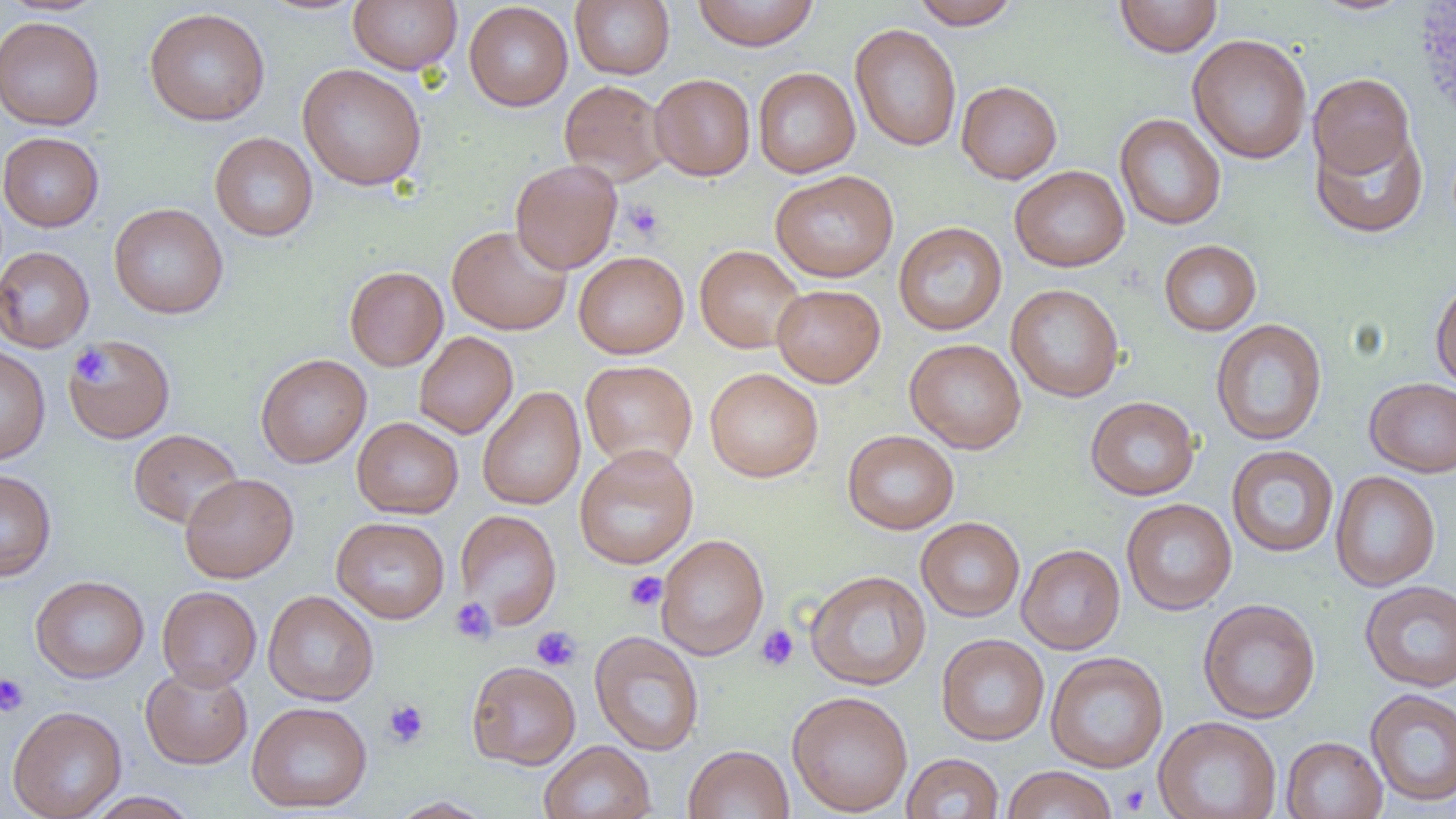

Approximate bounding boxes as (x1,y1)-(x2,y2) corner pairs in pixels. Uninfected red blood cell locations: (348,0)-(462,74), (691,0)-(820,51), (911,0)-(1020,29), (1114,0)-(1223,57), (1310,0)-(1417,16), (570,1)-(675,79), (463,2)-(573,111), (144,7)-(271,126), (1,15)-(104,131), (850,24)-(962,152), (1187,33)-(1312,165), (297,63)-(427,191), (753,67)-(860,178), (763,69)-(872,282), (1307,73)-(1415,179), (649,74)-(755,180), (559,79)-(669,185), (956,80)-(1062,183), (1115,113)-(1226,230), (1311,126)-(1427,238), (0,132)-(104,231), (209,132)-(318,242), (510,159)-(623,274), (1009,165)-(1130,272), (770,170)-(899,282), (108,203)-(229,319), (893,221)-(1007,336), (447,224)-(571,335), (1159,240)-(1262,336), (694,245)-(806,353), (0,246)-(94,353), (573,251)-(689,359), (344,265)-(448,371), (1430,277)-(1456,393), (1006,283)-(1125,402), (771,284)-(885,388), (1210,318)-(1327,446), (414,331)-(518,438), (63,335)-(177,444), (904,338)-(1026,453), (0,345)-(51,464), (255,353)-(371,468), (580,360)-(698,470), (704,368)-(823,482), (1364,377)-(1456,477), (477,386)-(586,511), (1085,396)-(1201,500), (352,417)-(464,519), (128,429)-(243,529), (842,429)-(959,534), (574,444)-(698,569), (1226,445)-(1339,558), (0,469)-(57,581), (1330,470)-(1441,591), (180,473)-(299,583), (1121,498)-(1237,615), (454,509)-(562,629), (331,516)-(450,623), (915,516)-(1025,621), (655,534)-(769,661), (1016,543)-(1125,654), (804,569)-(931,690), (30,575)-(149,683), (1359,579)-(1456,692), (157,586)-(262,690), (262,590)-(379,706), (1197,598)-(1321,724), (589,631)-(704,756), (936,633)-(1050,745), (1045,651)-(1168,773), (466,660)-(581,770), (141,664)-(253,769), (1365,688)-(1456,807), (787,690)-(913,817), (246,701)-(372,813), (7,705)-(126,819), (1153,716)-(1282,819), (1280,736)-(1387,819), (539,741)-(656,819), (683,744)-(795,819), (901,752)-(1004,818), (1001,765)-(1118,819), (86,791)-(200,818), (388,796)-(496,818). Platelet locations: (622,199)-(666,243), (70,345)-(113,386), (624,571)-(668,612), (449,597)-(497,645), (755,624)-(799,671), (530,626)-(581,671), (0,673)-(30,718), (382,699)-(429,748), (1118,782)-(1151,815). Slide-level diagnosis: negative for blood parasites. Thin blood film. Optical microscopy. 1000x magnification. Single field of view. Image is 1456×819 pixels.